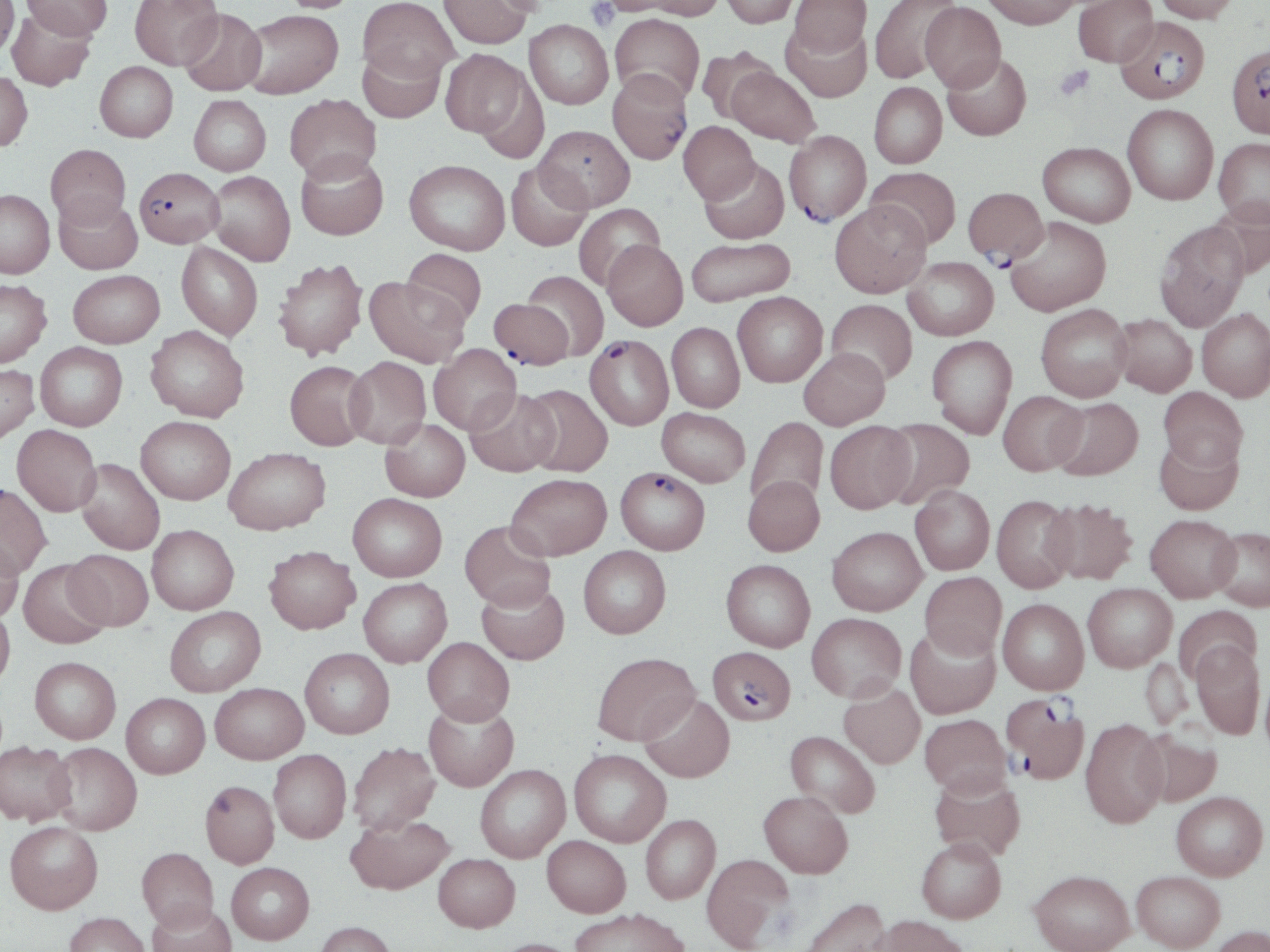
Summary:
  - Coordinate format: approximate bounding boxes as [x1, y1, x2, y2] in pixels
  - Plasmodium falciparum-infected red blood cell locations: [1115, 16, 1211, 104], [1227, 43, 1270, 137], [608, 69, 693, 164], [784, 131, 871, 226], [134, 166, 224, 247], [488, 298, 574, 369], [585, 334, 673, 430], [616, 467, 710, 555], [707, 646, 796, 725], [999, 693, 1092, 785]
  - Uninfected red blood cell locations: [0, 0, 19, 57], [22, 0, 112, 40], [129, 0, 222, 69], [280, 0, 362, 13], [358, 0, 458, 84], [439, 0, 532, 49], [600, 0, 684, 16], [720, 0, 798, 27], [790, 0, 870, 57], [869, 0, 960, 84], [981, 0, 1081, 29], [1072, 0, 1158, 67], [1154, 0, 1240, 23], [638, 1, 725, 20], [920, 2, 1006, 92], [6, 7, 95, 92], [179, 9, 266, 95], [242, 10, 343, 98], [610, 13, 705, 103], [525, 20, 613, 109], [781, 22, 871, 102], [358, 46, 445, 123], [696, 46, 777, 126], [440, 49, 529, 139], [942, 52, 1032, 141], [95, 61, 178, 142], [726, 65, 820, 147], [0, 72, 33, 151], [869, 82, 947, 169], [284, 94, 381, 182], [189, 95, 271, 176], [1122, 104, 1218, 205], [678, 121, 760, 204], [535, 125, 635, 211], [1213, 138, 1270, 227], [1038, 141, 1135, 227], [46, 144, 131, 227], [296, 151, 388, 240], [699, 158, 789, 244], [404, 159, 510, 255], [506, 162, 592, 251], [866, 166, 962, 249], [208, 171, 295, 266], [962, 187, 1048, 266], [0, 189, 54, 278], [53, 194, 142, 274], [1206, 199, 1270, 279], [830, 201, 931, 297], [573, 203, 665, 291], [1004, 217, 1111, 317], [1154, 221, 1250, 331], [686, 237, 795, 307], [603, 240, 688, 330], [177, 242, 263, 341], [401, 249, 487, 329], [903, 256, 998, 340], [273, 258, 368, 360], [68, 269, 164, 347], [522, 270, 609, 360], [364, 276, 468, 368], [0, 279, 51, 367], [733, 291, 828, 387], [826, 299, 917, 385], [1035, 304, 1131, 401], [1196, 308, 1270, 401], [1112, 313, 1197, 397], [667, 322, 745, 412], [146, 325, 249, 422], [926, 335, 1017, 438], [35, 342, 127, 431], [429, 344, 521, 434], [799, 347, 890, 429], [344, 356, 431, 449], [285, 360, 372, 450], [0, 363, 39, 445], [521, 384, 613, 477], [1159, 386, 1247, 472], [465, 389, 559, 476], [998, 390, 1087, 476], [1050, 397, 1143, 480], [657, 407, 750, 487], [136, 416, 235, 504], [746, 416, 828, 510], [380, 418, 470, 501], [879, 419, 975, 510], [825, 420, 916, 513], [12, 424, 101, 516], [1154, 433, 1243, 516], [224, 447, 330, 534], [76, 458, 165, 555], [507, 473, 612, 560], [743, 475, 824, 556], [0, 483, 52, 577], [910, 486, 994, 574], [347, 493, 447, 581], [992, 494, 1078, 592], [1042, 498, 1139, 584], [1145, 514, 1240, 602], [460, 520, 556, 611], [147, 524, 238, 614], [828, 526, 927, 615], [1210, 526, 1270, 611], [0, 536, 23, 622], [264, 546, 360, 633], [578, 546, 671, 638], [63, 549, 153, 631], [17, 558, 112, 648], [721, 559, 815, 652], [920, 571, 1007, 659], [359, 578, 452, 667], [476, 580, 569, 665], [1083, 583, 1177, 672], [998, 598, 1089, 695], [0, 605, 15, 688], [165, 606, 265, 697], [1174, 606, 1262, 682], [807, 612, 906, 702], [905, 625, 1000, 719], [422, 637, 515, 725], [1191, 641, 1265, 739], [299, 647, 394, 738], [592, 652, 699, 746], [30, 657, 121, 744], [210, 682, 308, 764], [839, 682, 925, 768], [121, 693, 209, 778], [639, 693, 735, 782], [423, 700, 519, 791], [919, 714, 1011, 796], [1080, 718, 1168, 828], [1136, 726, 1223, 807], [785, 730, 881, 818], [0, 740, 76, 826], [47, 742, 142, 835], [347, 742, 440, 835], [268, 749, 351, 843], [569, 749, 671, 847], [475, 764, 570, 862], [929, 773, 1026, 861], [200, 779, 279, 868], [759, 790, 853, 878], [1171, 791, 1268, 880], [345, 813, 454, 895], [640, 814, 720, 904], [4, 820, 103, 914], [542, 835, 631, 917], [916, 837, 1006, 923], [137, 847, 219, 931], [433, 853, 520, 932], [702, 853, 794, 951], [226, 862, 315, 944], [1029, 869, 1135, 952], [1132, 871, 1225, 951], [798, 897, 891, 952], [148, 902, 236, 952], [570, 907, 690, 952], [64, 911, 151, 952], [875, 915, 970, 952], [314, 921, 396, 952], [1208, 924, 1270, 952], [489, 937, 583, 952]
  - Platelet locations: [585, 0, 619, 31], [1054, 65, 1094, 99]
  - Slide-level diagnosis: Plasmodium falciparum
  - Field of view: one of a larger specimen
  - Modality: light microscopy
  - Stain: May-Grünwald-Giemsa
  - Magnification: 1000x
  - Preparation: thin blood smear
  - Image size: 1270×952 pixels